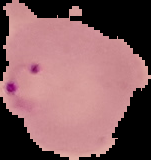 Image is 151×160 pixels. From a thin blood film. Segmented cell region on a black background. Result: Plasmodium parasites detected.